Assess this cell for malaria.
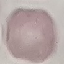

It is uninfected.

preparation: thin smear
stain: Giemsa
image_type: cell patch, automatically extracted from a larger field of view and resized to 64 × 64 pixels
capture: smartphone through the microscope eyepiece